Describe the morphology of the erythrocytes.
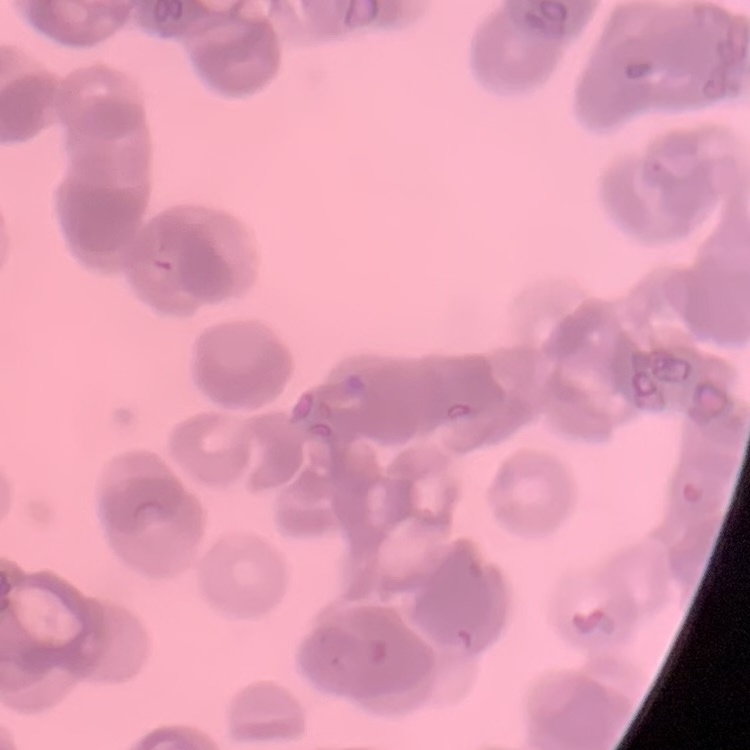

They show rouleaux formation.

Stained with either Field's or Giemsa. Thin peripheral smear. One tile cut from a larger photomicrograph.